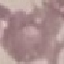
Summary:
  - Result: negative for malaria parasites
  - Stain: Giemsa
  - Preparation: thin smear
  - Capture: smartphone through the microscope eyepiece
  - Image type: automatically extracted cell patch, resized to 64 × 64 pixels